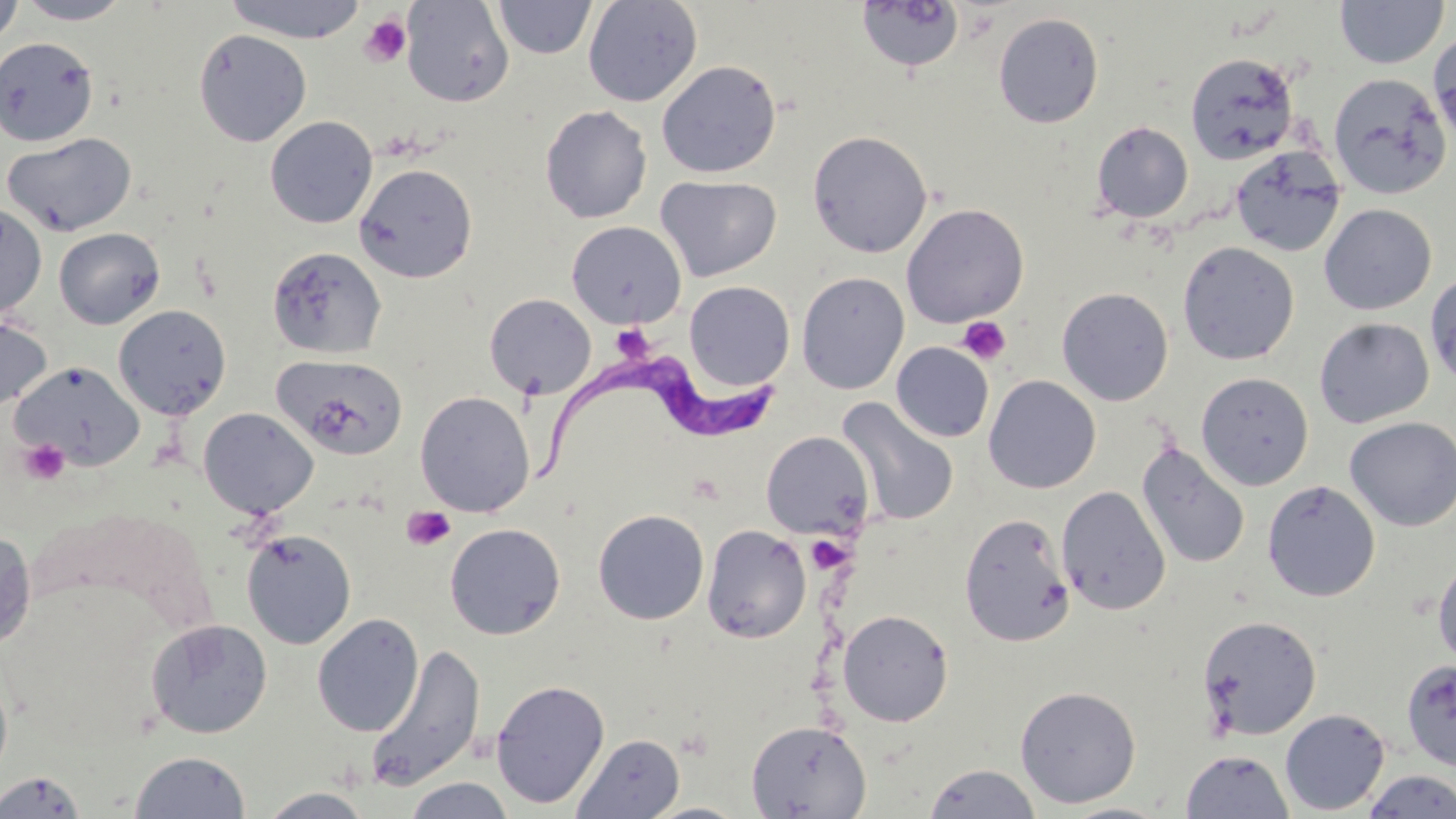
slide-level diagnosis = Trypanosoma brucei
stain = May-Grünwald-Giemsa
modality = light microscopy
platelet locations = approximate bounding boxes as (x1,y1)-(x2,y2) corner pairs in pixels: (359,15)-(411,67), (957,316)-(1011,365), (618,333)-(653,365), (18,439)-(70,485), (401,505)-(456,551), (811,541)-(854,574)
image size = 1456×819 pixels
preparation = thin blood smear
Trypanosoma brucei locations = approximate bounding boxes as (x1,y1)-(x2,y2) corner pairs in pixels: (530,352)-(776,482)
field of view = single
uninfected red blood cell locations = approximate bounding boxes as (x1,y1)-(x2,y2) corner pairs in pixels: (0,0)-(24,48), (13,0)-(134,25), (223,0)-(370,43), (401,0)-(514,108), (493,0)-(597,59), (582,0)-(703,107), (1335,0)-(1449,69), (856,2)-(965,73), (993,12)-(1104,128), (193,29)-(312,147), (1428,30)-(1456,146), (0,37)-(99,147), (1185,52)-(1300,164), (657,60)-(781,178), (1328,72)-(1453,199), (539,105)-(652,223), (265,116)-(378,228), (1091,121)-(1193,223), (807,130)-(933,258), (2,132)-(136,236), (1230,145)-(1346,257), (354,163)-(479,283), (655,175)-(781,281), (901,202)-(1029,327), (0,203)-(47,321), (1319,203)-(1437,315), (566,220)-(686,328), (53,227)-(165,329), (1177,241)-(1300,365), (267,247)-(387,360), (795,270)-(910,395), (1425,270)-(1456,391), (684,281)-(795,391), (1057,287)-(1174,406), (484,293)-(596,400), (113,304)-(232,419), (0,313)-(52,414), (1314,317)-(1434,429), (891,342)-(994,443), (273,354)-(409,461), (11,360)-(146,470), (1196,372)-(1314,490), (983,375)-(1101,494), (414,391)-(535,517), (837,398)-(959,527), (198,408)-(319,518), (1344,417)-(1456,531), (760,431)-(875,540), (1136,441)-(1250,569), (1262,480)-(1380,602), (1056,485)-(1171,615), (593,509)-(709,625), (959,512)-(1075,646), (444,522)-(566,640), (701,524)-(812,644), (0,529)-(36,651), (240,529)-(357,649), (1432,553)-(1456,671), (837,609)-(954,726), (312,613)-(424,736), (1198,614)-(1323,740), (145,619)-(272,738), (364,644)-(486,792), (1401,659)-(1456,772), (0,668)-(13,786), (490,679)-(610,809), (1014,685)-(1141,808), (1280,709)-(1390,815), (746,720)-(872,818), (572,733)-(684,818), (1180,749)-(1294,818), (128,750)-(251,818), (923,763)-(1041,818), (1361,770)-(1456,817), (0,771)-(87,817), (402,777)-(516,818), (258,787)-(375,818), (1057,801)-(1174,819)
magnification = 1000x